Classify this cell by malaria status.
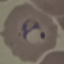
Parasitized.

Thin smear of blood. Automatically extracted cell patch, resized to 64 × 64 pixels. Giemsa stain. Acquired by smartphone through the microscope eyepiece.